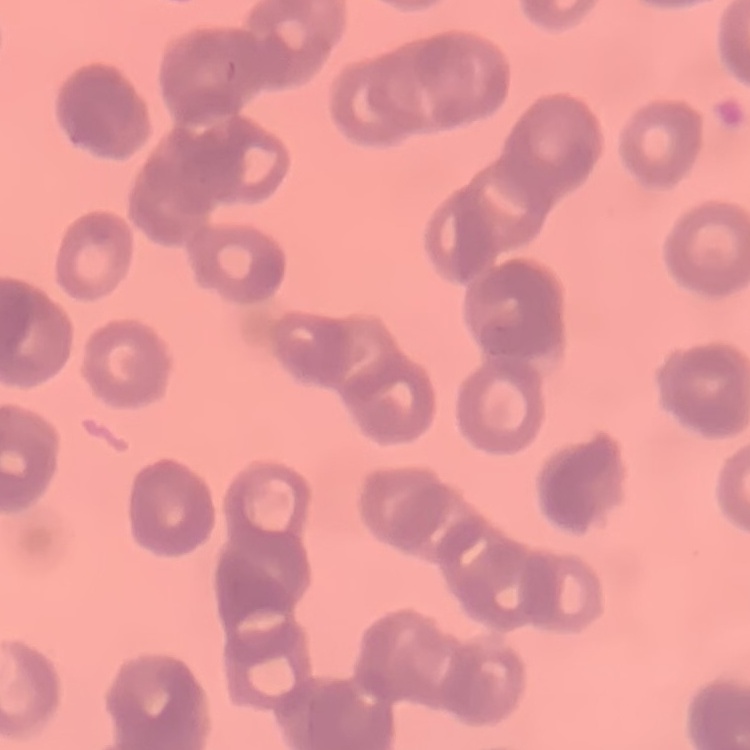

erythrocyte_morphology: rouleaux formation
image_type: square crop of a larger photomicrograph
stain: Field's or Giemsa
preparation: thin blood smear